Outline each Plasmodium falciparum-infected red blood cell.
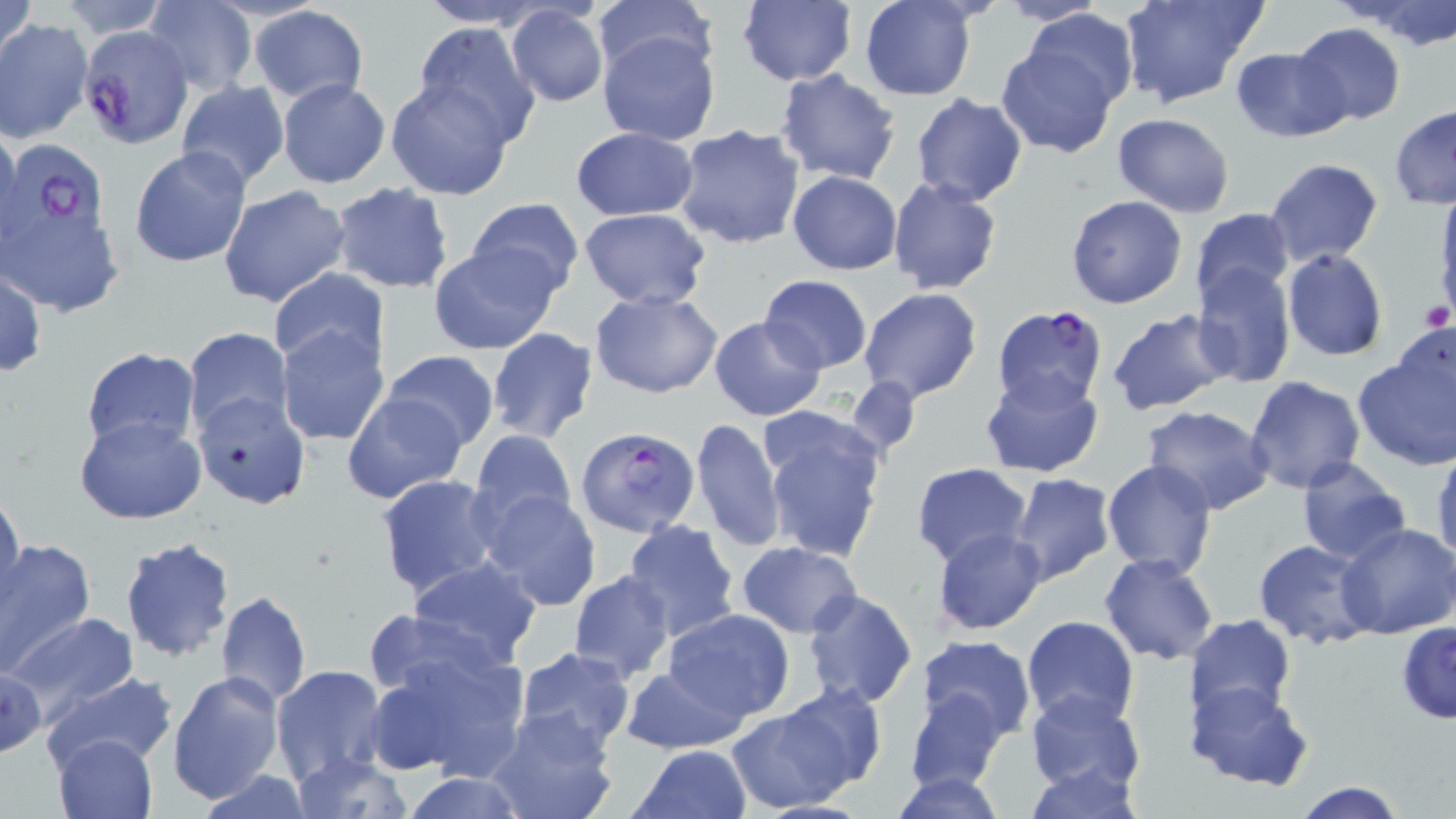

Approximate bounding boxes as (x1,y1)-(x2,y2) corner pairs in pixels.
Plasmodium falciparum-infected red blood cells: (80,26)-(200,152), (0,136)-(106,246), (995,308)-(1115,416), (575,429)-(702,541).

Platelet locations: (1417,299)-(1452,333). Uninfected red blood cell locations: (1,0)-(38,71), (53,0)-(172,38), (414,0)-(552,28), (589,0)-(719,82), (736,0)-(857,88), (1118,0)-(1264,109), (1347,0)-(1456,47), (143,1)-(256,92), (859,1)-(978,101), (991,1)-(1111,26), (505,4)-(611,107), (248,5)-(369,105), (1023,8)-(1138,115), (1,18)-(92,143), (410,21)-(542,146), (1290,23)-(1406,127), (597,29)-(721,146), (996,44)-(1120,157), (1231,48)-(1347,142), (642,54)-(791,219), (775,70)-(902,185), (385,79)-(513,199), (175,80)-(289,191), (277,80)-(390,188), (910,92)-(1029,206), (1389,105)-(1456,209), (1112,112)-(1235,217), (672,124)-(805,249), (0,126)-(24,255), (571,126)-(699,221), (128,146)-(254,267), (1263,158)-(1384,267), (787,171)-(903,275), (886,176)-(1003,295), (876,180)-(992,400), (329,182)-(454,294), (218,185)-(350,309), (1434,191)-(1456,321), (467,196)-(584,299), (1065,196)-(1187,309), (577,208)-(710,309), (1190,208)-(1296,308), (5,213)-(122,311), (429,244)-(559,355), (1281,249)-(1387,363), (1191,262)-(1295,387), (0,266)-(47,379), (269,269)-(388,371), (759,275)-(871,374), (858,287)-(982,403), (590,289)-(724,398), (1106,308)-(1234,416), (709,315)-(826,422), (276,324)-(389,447), (486,327)-(599,443), (182,328)-(293,441), (1353,337)-(1455,473), (81,347)-(201,455), (382,349)-(500,451), (978,369)-(1104,479), (843,375)-(927,456), (1244,377)-(1366,495), (192,390)-(312,511), (342,390)-(468,504), (1142,405)-(1276,515), (758,411)-(889,564), (74,415)-(207,524), (692,417)-(786,551), (468,429)-(577,536), (1431,444)-(1456,565), (1294,457)-(1411,565), (1101,459)-(1218,579), (911,463)-(1034,568), (374,473)-(500,600), (1008,474)-(1118,588), (476,489)-(603,613), (0,490)-(24,610), (622,518)-(741,642), (1336,523)-(1456,639), (933,528)-(1048,635), (119,536)-(235,664), (1252,536)-(1377,648), (0,539)-(97,677), (736,540)-(862,637), (1099,553)-(1219,665), (408,556)-(545,667), (568,570)-(676,683), (802,588)-(918,710), (215,591)-(310,708), (360,600)-(515,700), (661,609)-(796,720), (8,613)-(140,722), (1186,615)-(1297,728), (1022,617)-(1140,731), (1397,621)-(1455,723), (917,636)-(1036,742), (366,640)-(530,783), (513,647)-(637,755), (619,664)-(749,755), (0,665)-(50,760), (270,665)-(390,790), (168,670)-(285,806), (41,671)-(178,772), (1184,680)-(1313,790), (772,685)-(885,798), (904,687)-(1009,793), (1025,689)-(1147,799), (725,703)-(857,813), (483,706)-(621,819), (53,733)-(159,819), (626,743)-(755,819), (290,750)-(413,819), (1020,763)-(1149,817), (892,770)-(1010,818), (401,774)-(528,818), (1289,780)-(1409,819). Slide-level diagnosis: Plasmodium falciparum. 1000x magnification. Optical microscopy. Thin blood smear. One field of a larger specimen. Image is 1456×819 pixels. May-Grünwald-Giemsa stain.